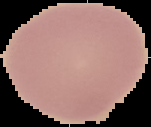
Summary:
  - Image size: 151×127 pixels
  - Image type: cell region segmented out of the field of view; surrounding area masked to black
  - Result: no malaria parasites detected
  - Preparation: thin blood smear